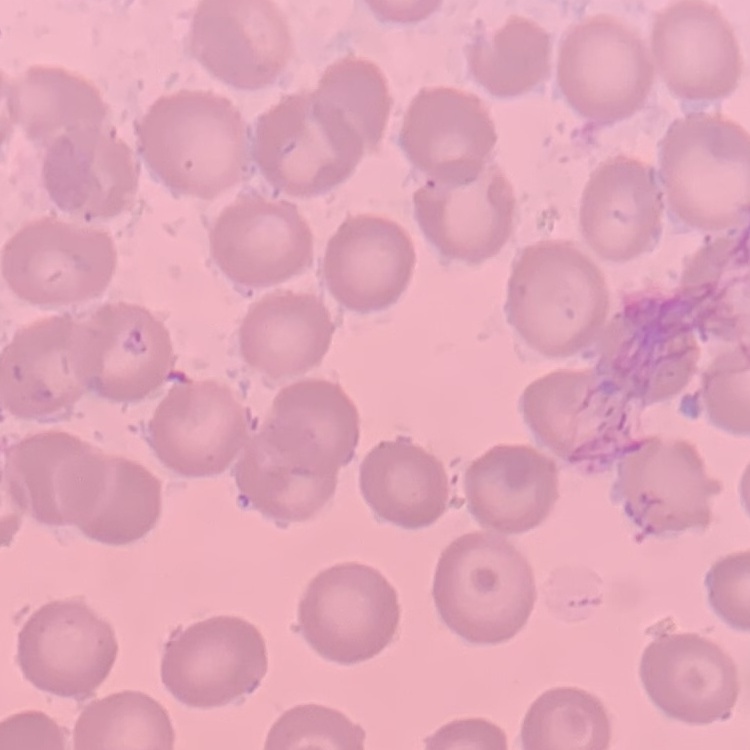

erythrocyte morphology = no rouleaux formation
image type = square crop of a larger photomicrograph
stain = Field's or Giemsa
preparation = thin peripheral smear